State the blood parasite species.
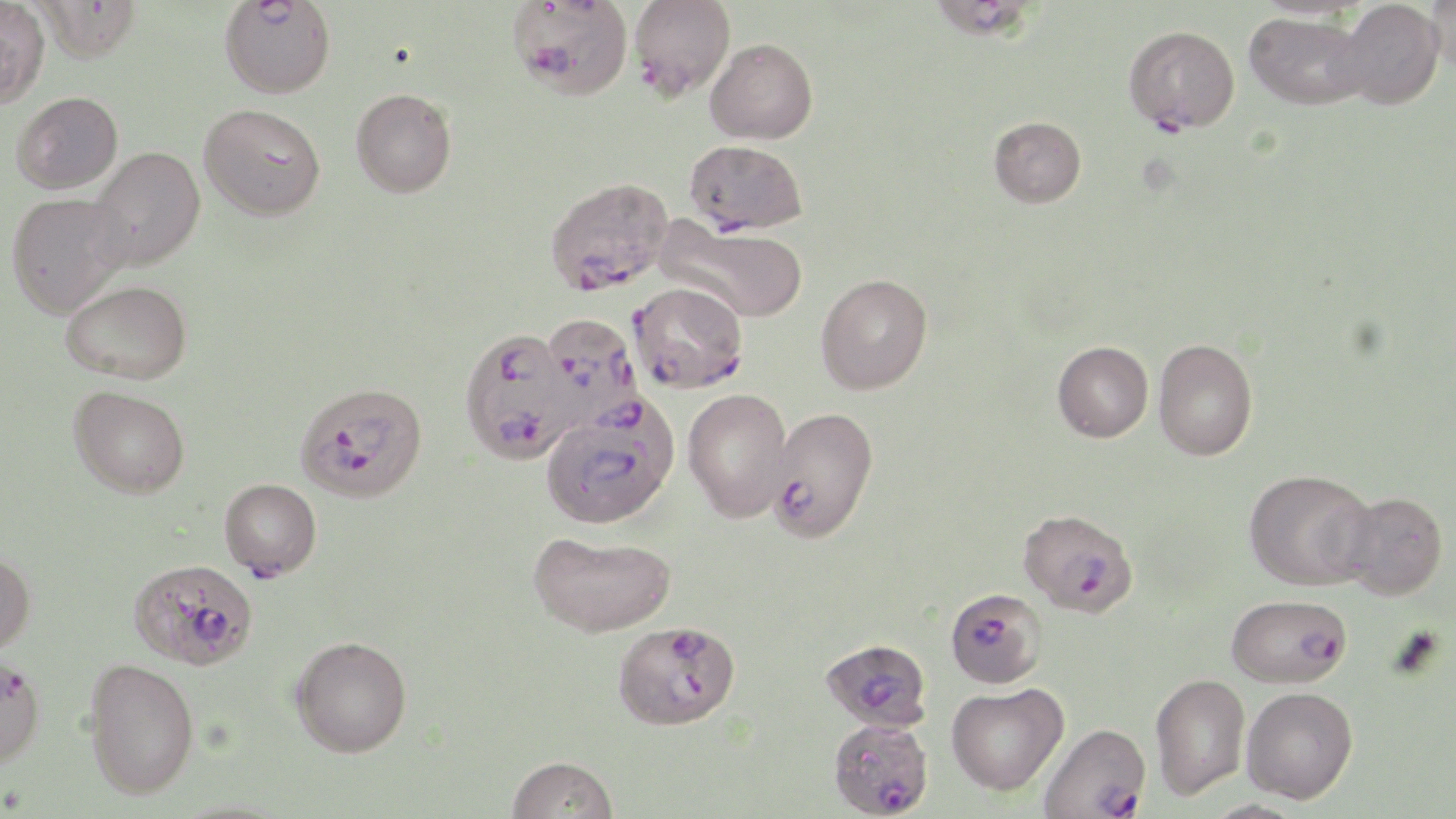

Plasmodium falciparum.

Summary:
  - Coordinate format: approximate bounding boxes as [x1, y1, x2, y2] in pixels
  - Uninfected red blood cell locations: [1336, 0, 1445, 109], [1428, 0, 1456, 76], [0, 1, 50, 108], [1244, 11, 1368, 110], [705, 37, 818, 144], [350, 87, 456, 197], [12, 91, 123, 193], [199, 103, 326, 221], [989, 115, 1086, 207], [86, 146, 206, 272], [6, 192, 130, 318], [656, 218, 808, 324], [816, 273, 932, 394], [61, 280, 192, 383], [1152, 338, 1258, 460], [1052, 341, 1153, 442], [70, 385, 190, 497], [682, 388, 794, 523], [1244, 468, 1378, 591], [1339, 491, 1448, 600], [528, 530, 676, 637], [0, 551, 35, 656], [290, 636, 412, 757], [83, 658, 198, 799], [1150, 672, 1250, 800], [946, 682, 1069, 796], [1241, 686, 1358, 803], [506, 755, 618, 818], [1200, 799, 1311, 819]
  - Plasmodium falciparum-infected red blood cell locations: [219, 0, 335, 98], [508, 0, 632, 101], [629, 0, 735, 101], [937, 0, 1032, 42], [34, 1, 142, 62], [1123, 24, 1240, 134], [685, 139, 807, 235], [545, 176, 673, 295], [629, 282, 749, 393], [541, 312, 642, 429], [459, 328, 579, 465], [294, 381, 428, 502], [541, 395, 680, 529], [766, 407, 879, 543], [219, 478, 322, 579], [1018, 507, 1138, 616], [132, 567, 254, 670], [945, 588, 1047, 689], [1226, 594, 1352, 688], [613, 620, 741, 730], [820, 638, 932, 732], [0, 653, 45, 770], [827, 718, 934, 818], [1038, 722, 1151, 819]
  - Field of view: single
  - Preparation: thin blood film
  - Stain: May-Grünwald-Giemsa
  - Magnification: 1000x
  - Modality: optical microscopy
  - Image size: 1456×819 pixels